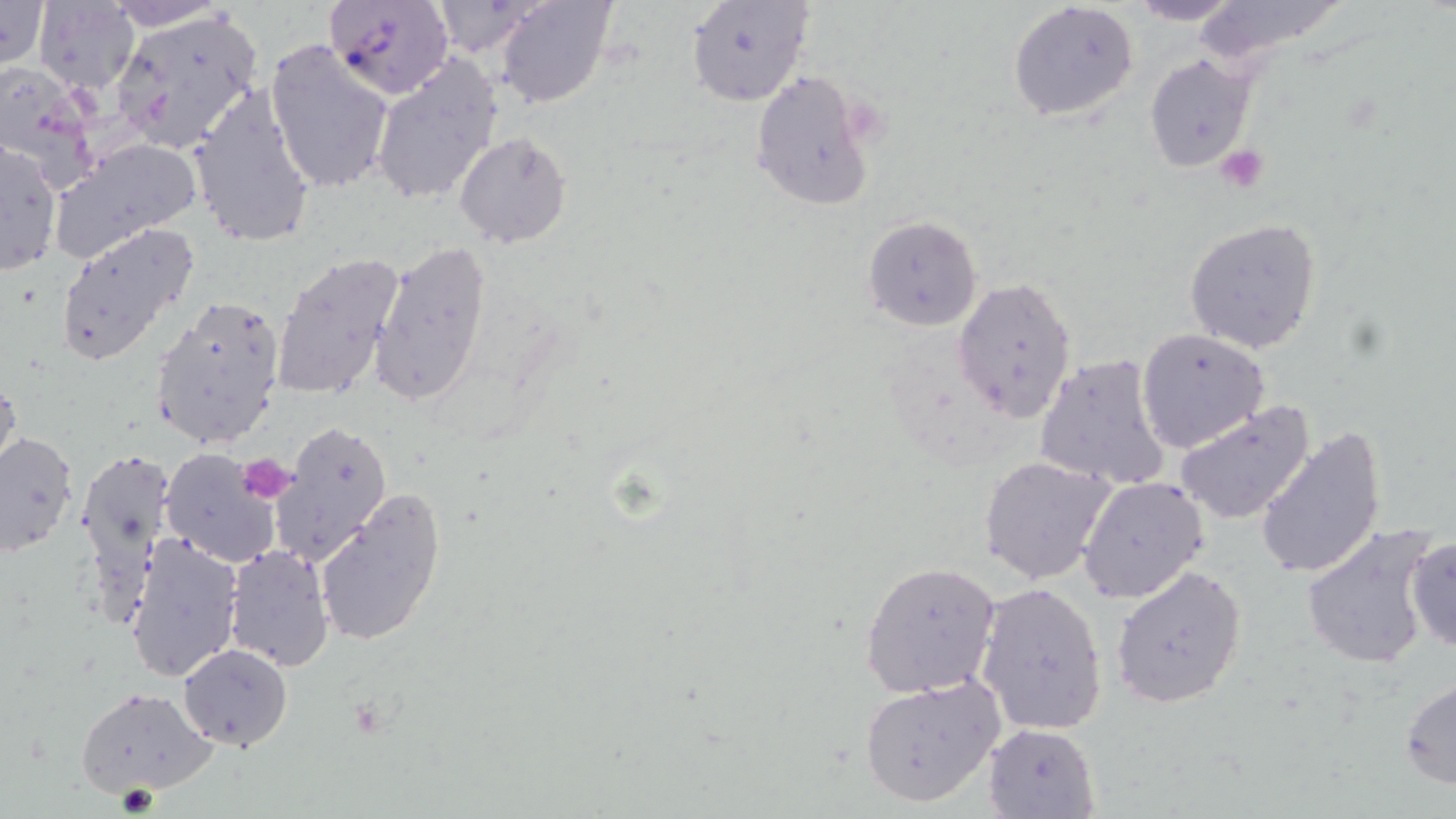
{
  "slide_level_diagnosis": "Plasmodium falciparum",
  "platelet_locations": "approximate bounding boxes as (x1,y1)-(x2,y2) corner pairs in pixels: (1216,143)-(1271,192), (242,452)-(296,503)",
  "magnification": "1000x",
  "stain": "May-Grünwald-Giemsa",
  "preparation": "thin blood film",
  "plasmodium_falciparum_infected_red_blood_cell_locations": "approximate bounding boxes as (x1,y1)-(x2,y2) corner pairs in pixels: (324,0)-(456,99)",
  "image_size": "1456×819 pixels",
  "modality": "optical microscopy",
  "field_of_view": "one of a larger specimen",
  "uninfected_red_blood_cell_locations": "approximate bounding boxes as (x1,y1)-(x2,y2) corner pairs in pixels: (0,0)-(50,75), (101,0)-(235,31), (494,0)-(618,109), (684,0)-(814,108), (1124,0)-(1245,24), (1183,0)-(1357,67), (33,1)-(141,95), (425,1)-(552,57), (1008,1)-(1139,123), (110,7)-(266,155), (263,38)-(395,194), (1144,52)-(1257,174), (370,56)-(503,206), (0,61)-(103,189), (749,69)-(878,211), (187,85)-(318,251), (453,132)-(572,249), (1,137)-(62,279), (48,138)-(201,263), (861,214)-(982,333), (1183,218)-(1323,353), (55,220)-(200,367), (368,238)-(492,410), (270,251)-(408,405), (952,276)-(1078,423), (152,296)-(285,450), (1136,328)-(1270,452), (1034,352)-(1172,492), (0,374)-(21,487), (1175,399)-(1317,525), (271,422)-(393,563), (1254,424)-(1386,580), (1,431)-(77,557), (160,446)-(281,569), (75,452)-(173,630), (977,455)-(1118,586), (1079,476)-(1210,604), (314,487)-(447,648), (1301,525)-(1441,670), (121,531)-(245,685), (1404,535)-(1456,656), (222,545)-(334,672), (860,561)-(1002,698), (1109,565)-(1248,707), (975,582)-(1108,736), (178,643)-(292,748), (1400,675)-(1456,791), (858,677)-(1006,808), (77,685)-(218,798), (983,723)-(1100,817)"
}